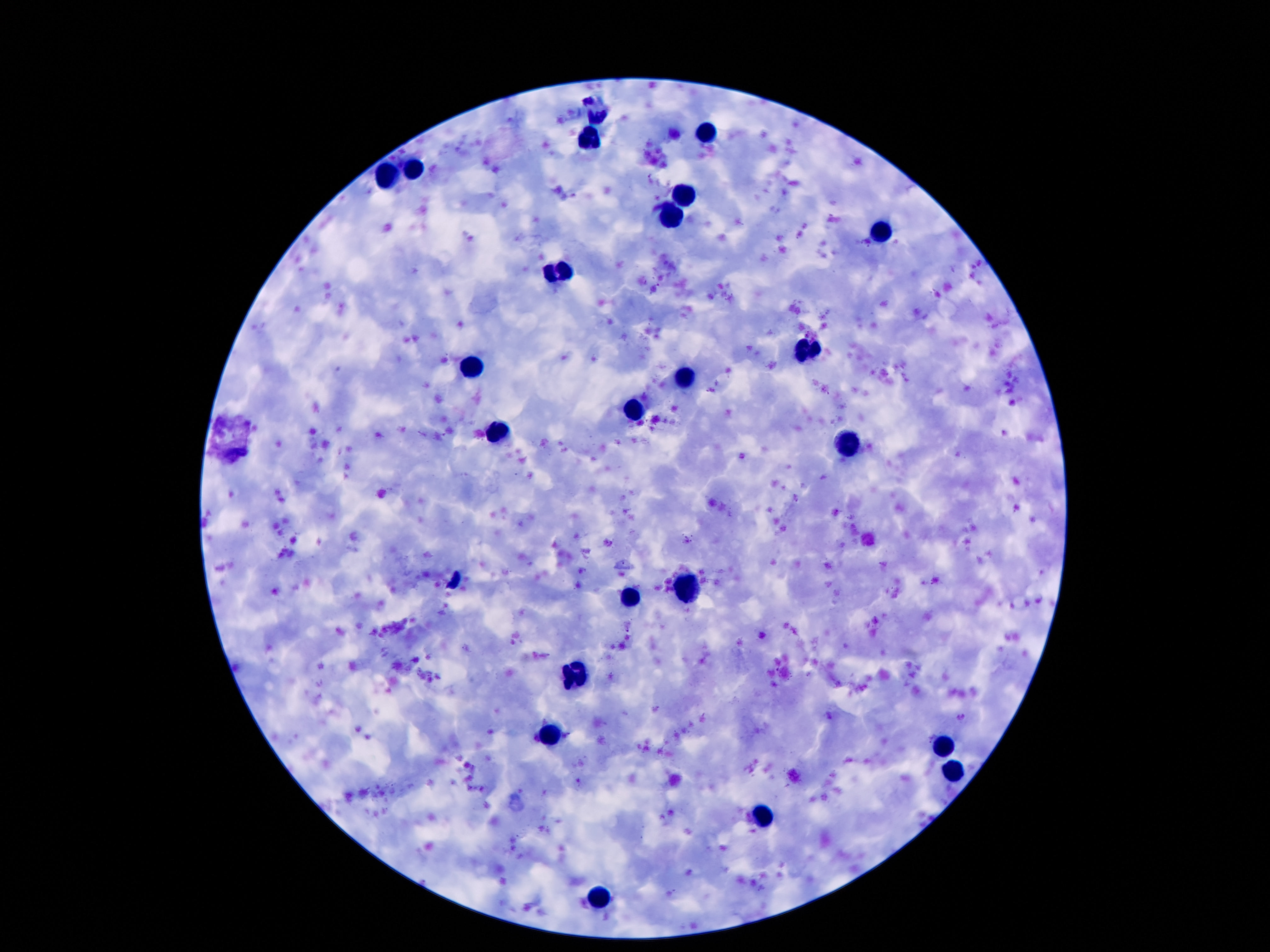
Approximate object centers, in pixels from the top-left corner. Leukocyte locations: (x=705, y=134), (x=590, y=140), (x=411, y=169), (x=386, y=176), (x=682, y=195), (x=667, y=218), (x=880, y=232), (x=556, y=271), (x=808, y=351), (x=466, y=367), (x=686, y=376), (x=634, y=412), (x=501, y=433), (x=846, y=445), (x=688, y=591), (x=630, y=597), (x=575, y=673), (x=550, y=733), (x=947, y=742), (x=953, y=776), (x=760, y=813), (x=600, y=897). Single field of view. Image is 1270×952 pixels. 100x magnification. Thick blood film. Photographed through the microscope eyepiece with a smartphone camera. Patient malaria status: uninfected. Giemsa-stained preparation.